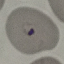
Malaria status: parasitized. Thin smear of blood. Automatically extracted cell patch, resized to 64 × 64 pixels. Photographed with a smartphone camera at the microscope eyepiece. Giemsa-stained preparation.